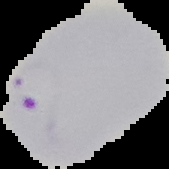
preparation: thin blood film
image_size: 169×169 pixels
malaria_status: parasitized
image_type: cell region segmented out of the field of view; surrounding area masked to black